Give the position of every Plasmodium parasite.
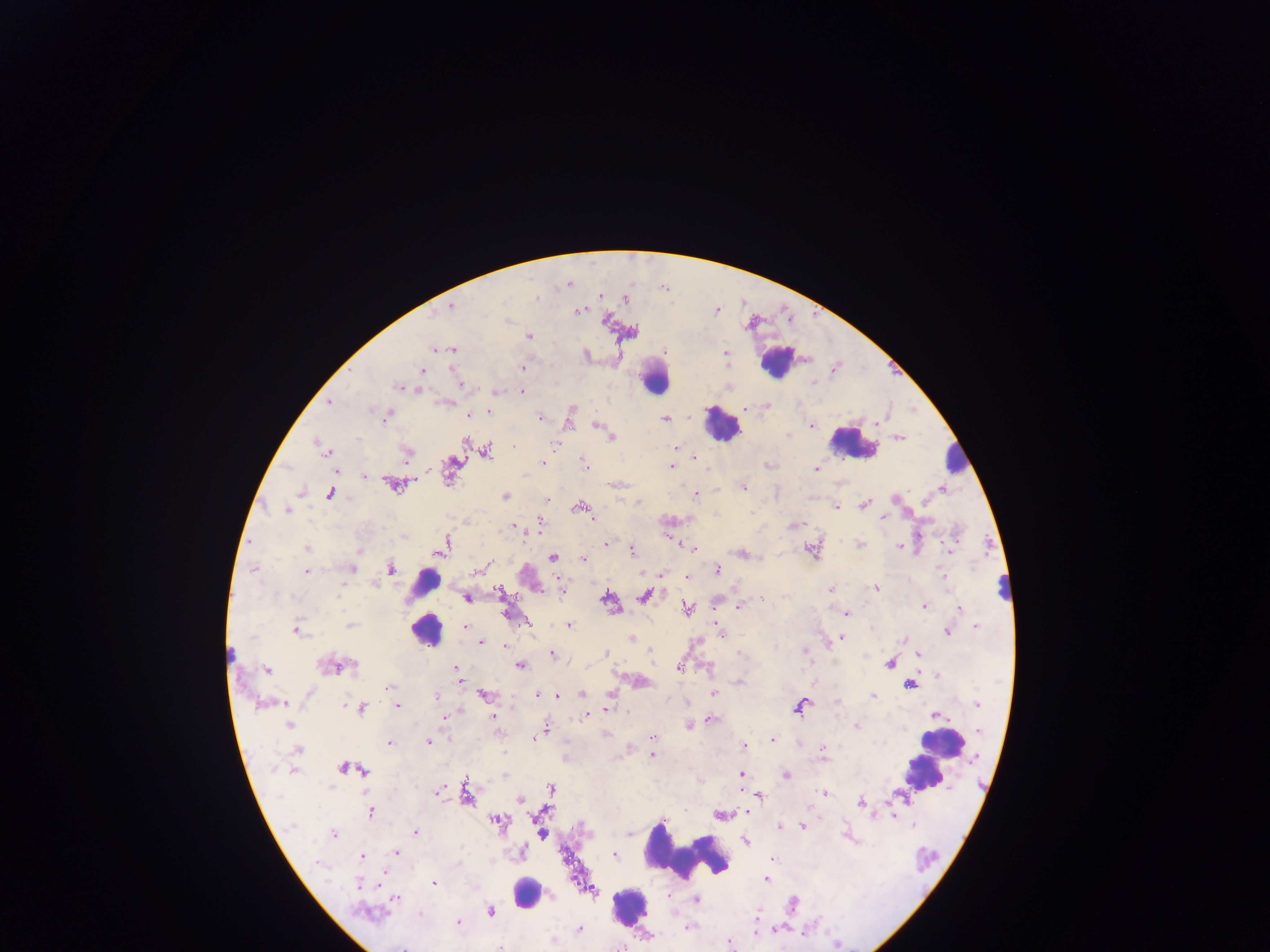

Approximate centers as (x, y) in pixels.
Plasmodium parasites: (568, 284), (600, 295), (536, 298), (625, 299), (451, 306), (580, 310), (715, 311), (529, 336), (435, 348), (452, 349), (726, 351), (523, 367), (422, 370), (814, 382), (460, 384), (398, 387), (416, 390), (522, 393), (330, 402), (766, 405), (371, 411), (489, 412), (469, 415), (387, 416), (541, 417), (664, 418), (568, 423), (598, 426), (812, 426), (610, 436), (788, 436), (899, 437), (315, 442), (466, 443), (554, 445), (321, 446), (675, 447), (486, 451), (327, 452), (407, 453), (696, 456), (543, 462), (585, 463), (671, 466), (816, 469), (335, 471), (365, 476), (393, 485), (744, 487), (942, 490), (301, 493), (330, 494), (696, 494), (505, 496), (545, 499), (894, 499), (639, 502), (864, 504), (580, 507), (836, 507), (287, 509), (751, 512), (587, 513), (593, 517), (883, 518), (540, 520), (514, 525), (795, 526), (403, 537), (861, 543), (608, 544), (899, 546), (442, 547), (306, 548), (693, 549), (631, 550), (950, 551), (741, 554), (552, 558), (583, 559), (488, 563), (390, 568), (253, 569), (352, 569), (476, 570), (717, 570), (306, 572), (687, 576), (944, 578), (376, 585), (875, 588), (831, 589), (500, 592), (337, 596), (645, 596), (466, 597), (606, 598), (762, 600), (925, 606), (738, 607), (687, 609), (959, 609), (846, 613), (350, 625), (569, 625), (465, 626), (717, 627), (976, 627), (872, 629), (297, 631), (719, 632), (948, 632), (631, 638), (843, 638), (480, 642), (504, 646), (650, 650), (804, 650), (606, 652), (741, 653), (551, 654), (918, 654), (889, 663), (521, 665), (330, 666), (351, 666), (678, 667), (455, 669), (266, 670), (938, 676), (738, 683), (910, 684), (389, 687), (583, 694), (609, 694), (713, 694), (484, 695), (537, 695), (558, 696), (873, 696), (436, 697), (837, 702), (283, 703), (345, 705), (398, 705), (977, 705), (800, 707), (362, 708), (609, 710), (586, 715), (935, 715), (444, 717), (494, 717), (711, 719), (288, 725), (688, 725), (856, 726), (545, 731), (979, 731), (538, 737), (652, 738), (534, 739), (772, 739), (429, 741), (389, 744), (744, 746), (823, 749), (298, 750), (823, 754), (652, 756), (343, 768), (362, 771), (741, 774), (785, 775), (503, 776), (551, 788), (437, 792), (466, 793), (822, 793), (760, 796), (520, 799), (861, 803), (371, 812), (746, 813), (721, 814), (894, 815), (498, 821), (913, 825), (291, 826), (780, 826), (802, 826), (415, 832), (542, 833), (334, 834), (629, 834), (744, 841), (396, 852), (522, 852), (615, 856), (361, 857), (773, 859), (318, 863), (766, 879), (434, 883), (359, 884), (551, 896), (669, 896), (396, 898), (696, 900), (366, 912), (490, 912), (420, 914), (757, 916), (458, 923), (688, 927), (579, 930), (757, 932), (552, 941), (729, 944), (837, 945).

Summary:
  - Leukocyte locations (subset; some below the resolvable size): (777, 362), (654, 379), (721, 425), (854, 444), (958, 455), (427, 583), (1007, 586), (426, 630), (231, 653), (942, 745), (918, 771), (688, 853), (526, 892), (630, 907)
  - Field of view: single
  - Capture: mobile-phone photograph through a microscope
  - Country: Ghana
  - Image size: 1270×952 pixels
  - Preparation: thick blood film